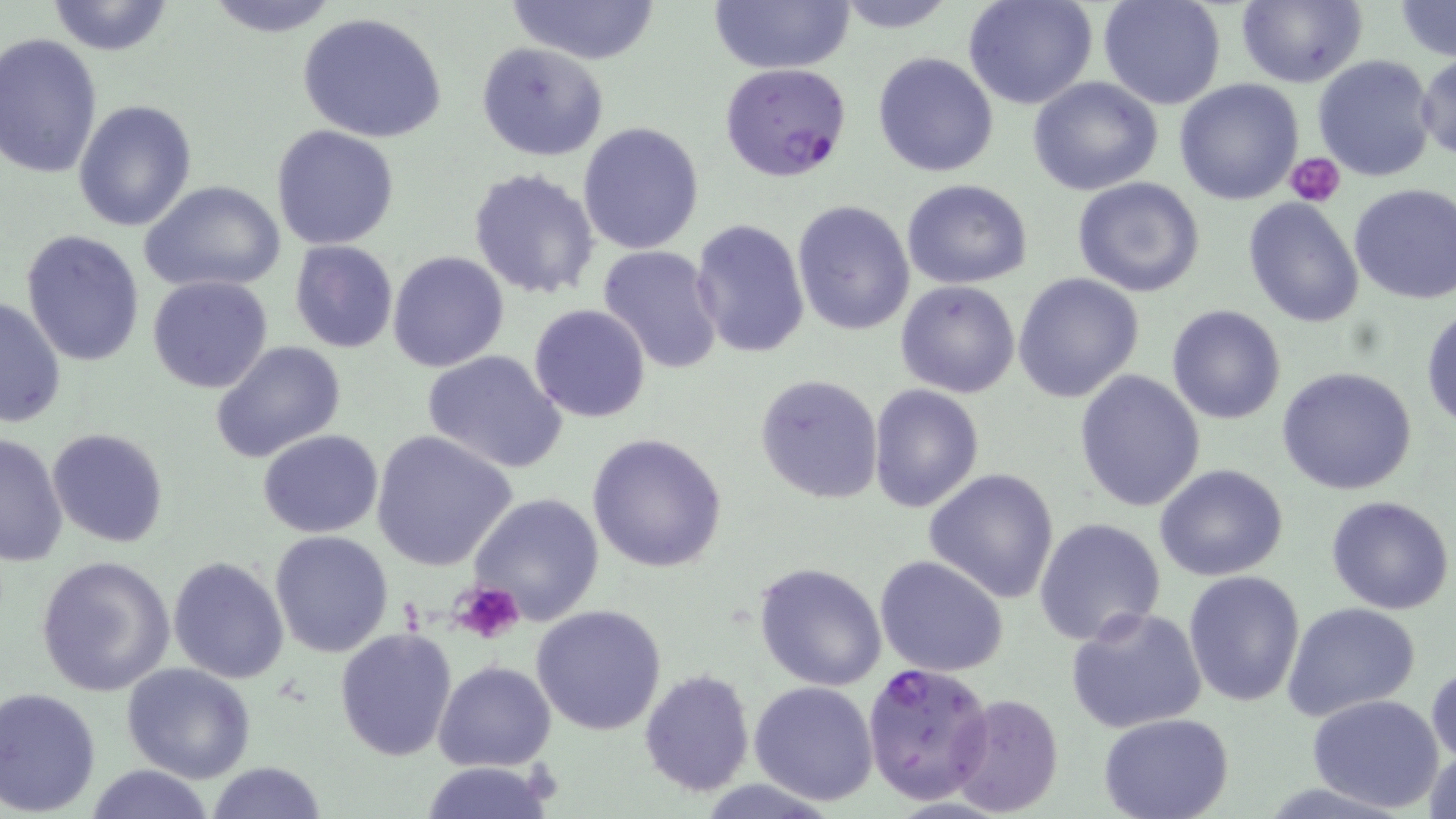

{
  "slide_level_diagnosis": "Plasmodium falciparum",
  "modality": "optical microscopy",
  "preparation": "thin blood film",
  "field_of_view": "single",
  "stain": "May-Grünwald-Giemsa",
  "magnification": "1000x",
  "image_size": "1456×819 pixels",
  "plasmodium_falciparum_infected_red_blood_cell_locations": "approximate bounding boxes as named x1/y1/x2/y2 corners in pixels: (x1=718, y1=62, x2=852, y2=182), (x1=862, y1=662, x2=994, y2=801)",
  "uninfected_red_blood_cell_locations": "approximate bounding boxes as named x1/y1/x2/y2 corners in pixels: (x1=202, y1=0, x2=346, y2=38), (x1=504, y1=0, x2=662, y2=65), (x1=708, y1=0, x2=855, y2=73), (x1=827, y1=0, x2=961, y2=32), (x1=964, y1=0, x2=1097, y2=110), (x1=1097, y1=0, x2=1224, y2=110), (x1=1235, y1=0, x2=1367, y2=88), (x1=44, y1=1, x2=176, y2=55), (x1=1393, y1=2, x2=1456, y2=60), (x1=298, y1=11, x2=449, y2=143), (x1=0, y1=32, x2=103, y2=183), (x1=475, y1=43, x2=609, y2=162), (x1=872, y1=51, x2=999, y2=177), (x1=1366, y1=52, x2=1456, y2=170), (x1=1416, y1=52, x2=1456, y2=163), (x1=1312, y1=54, x2=1436, y2=182), (x1=1026, y1=76, x2=1162, y2=195), (x1=1174, y1=79, x2=1305, y2=205), (x1=73, y1=99, x2=196, y2=231), (x1=577, y1=120, x2=705, y2=254), (x1=271, y1=124, x2=401, y2=249), (x1=468, y1=167, x2=599, y2=300), (x1=1071, y1=177, x2=1205, y2=297), (x1=902, y1=179, x2=1032, y2=288), (x1=140, y1=181, x2=286, y2=295), (x1=1348, y1=182, x2=1456, y2=305), (x1=1242, y1=196, x2=1366, y2=327), (x1=791, y1=199, x2=915, y2=335), (x1=691, y1=218, x2=811, y2=361), (x1=21, y1=229, x2=147, y2=365), (x1=288, y1=240, x2=399, y2=352), (x1=597, y1=245, x2=725, y2=373), (x1=387, y1=250, x2=509, y2=372), (x1=1012, y1=272, x2=1144, y2=404), (x1=147, y1=275, x2=273, y2=393), (x1=896, y1=281, x2=1021, y2=399), (x1=1, y1=297, x2=67, y2=427), (x1=528, y1=304, x2=652, y2=423), (x1=1166, y1=304, x2=1286, y2=425), (x1=1421, y1=306, x2=1455, y2=431), (x1=210, y1=341, x2=348, y2=464), (x1=421, y1=349, x2=567, y2=473), (x1=1277, y1=367, x2=1420, y2=497), (x1=1074, y1=368, x2=1206, y2=511), (x1=755, y1=372, x2=885, y2=505), (x1=868, y1=384, x2=984, y2=512), (x1=47, y1=427, x2=170, y2=548), (x1=258, y1=430, x2=383, y2=538), (x1=370, y1=430, x2=519, y2=570), (x1=0, y1=431, x2=69, y2=567), (x1=586, y1=433, x2=729, y2=573), (x1=1155, y1=463, x2=1288, y2=582), (x1=923, y1=466, x2=1060, y2=603), (x1=465, y1=492, x2=607, y2=627), (x1=1326, y1=494, x2=1455, y2=615), (x1=1033, y1=516, x2=1167, y2=647), (x1=269, y1=531, x2=394, y2=657), (x1=35, y1=554, x2=177, y2=697), (x1=875, y1=555, x2=1009, y2=677), (x1=168, y1=556, x2=289, y2=684), (x1=752, y1=561, x2=887, y2=691), (x1=1183, y1=570, x2=1307, y2=708), (x1=1281, y1=601, x2=1421, y2=721), (x1=530, y1=603, x2=667, y2=736), (x1=1065, y1=606, x2=1207, y2=735), (x1=333, y1=626, x2=458, y2=762), (x1=433, y1=660, x2=556, y2=770), (x1=1427, y1=660, x2=1456, y2=771), (x1=121, y1=663, x2=257, y2=784), (x1=638, y1=669, x2=755, y2=795), (x1=748, y1=679, x2=878, y2=806), (x1=0, y1=687, x2=102, y2=816), (x1=1306, y1=692, x2=1444, y2=811), (x1=948, y1=693, x2=1065, y2=816), (x1=1098, y1=714, x2=1235, y2=819), (x1=1424, y1=742, x2=1455, y2=819), (x1=205, y1=760, x2=328, y2=818), (x1=418, y1=760, x2=557, y2=818), (x1=83, y1=764, x2=217, y2=819)",
  "platelet_locations": "approximate bounding boxes as named x1/y1/x2/y2 corners in pixels: (x1=1286, y1=153, x2=1345, y2=206), (x1=450, y1=581, x2=526, y2=645)"
}